Classify this cell by malaria status.
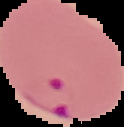
It is parasitized.

From a thin blood smear. Image is 124×127 pixels. The area outside the segmented cell region is set to black.